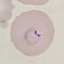 Result: malaria parasites identified. Cell patch, automatically extracted from a larger field of view and resized to 64 × 64 pixels. Thin smear of blood. Giemsa-stained preparation. Photographed with a smartphone camera at the microscope eyepiece.